Classify this cell by malaria status.
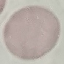

It is uninfected.

Summary:
  - Stain: Giemsa
  - Image type: automatically extracted cell patch, resized to 64 × 64 pixels
  - Preparation: thin blood smear
  - Capture: smartphone camera at the microscope eyepiece